Which red blood cells are Plasmodium falciparum-infected, and which are of indeterminate infection status?
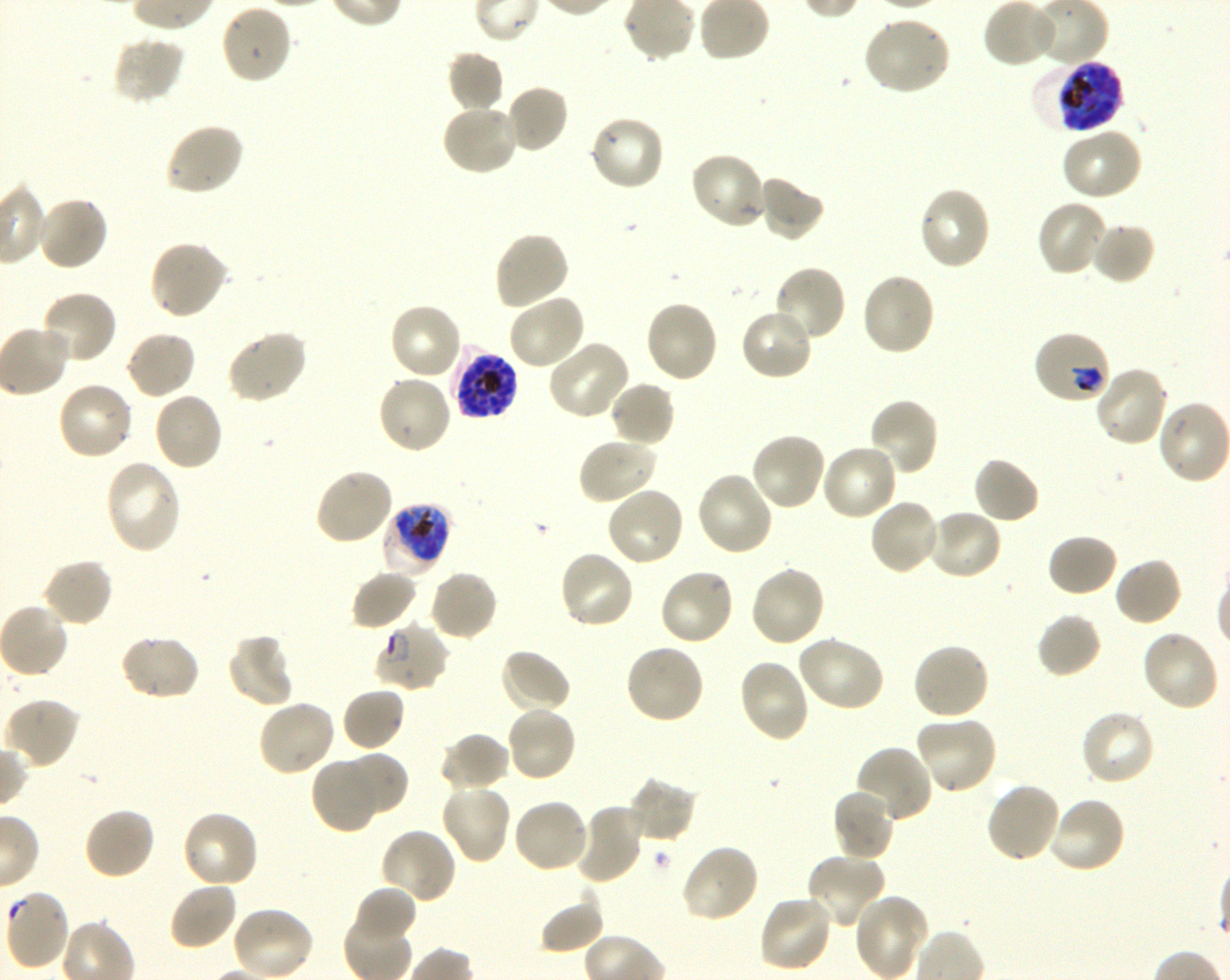

Approximate bounding boxes as [x1, y1, x2, y2] in pixels. Not every red blood cell is marked. A life-cycle stage — or a range of stages, where the recorded stages span more than one — follows each staged infected red blood cell.
Infected red blood cells: [1034, 58, 1124, 134] late trophozoite to late schizont; [1032, 330, 1112, 406] early trophozoite to early schizont; [453, 349, 518, 420] schizont; [380, 504, 451, 579] late trophozoite to late schizont; [373, 622, 450, 693] early ring to late trophozoite.
Red blood cells of indeterminate infection status: [2, 890, 69, 974].

locations of uninfected red blood cells = [220, 3, 294, 85], [862, 14, 952, 97], [112, 36, 186, 106], [447, 51, 504, 114], [503, 84, 569, 155], [441, 102, 519, 177], [588, 114, 666, 192], [164, 122, 245, 197], [1060, 127, 1143, 201], [687, 152, 767, 231], [757, 174, 825, 242], [917, 186, 993, 272], [34, 194, 109, 272], [1035, 199, 1111, 278], [1091, 221, 1156, 285], [493, 230, 570, 311], [148, 239, 229, 320], [772, 265, 847, 343], [860, 271, 936, 358], [39, 290, 118, 368], [506, 291, 587, 371], [643, 300, 719, 384], [388, 301, 464, 381], [739, 308, 814, 382], [125, 329, 197, 400], [226, 329, 308, 404], [546, 338, 632, 421], [1092, 365, 1170, 448], [376, 374, 454, 455], [55, 380, 134, 462], [608, 380, 676, 449], [151, 391, 224, 472], [867, 397, 939, 477], [750, 432, 828, 512], [577, 436, 658, 505], [819, 443, 898, 522], [971, 456, 1041, 525], [103, 459, 182, 554], [313, 466, 395, 546], [695, 471, 774, 557], [605, 485, 686, 568], [868, 497, 941, 575], [925, 507, 1003, 581], [1046, 532, 1119, 598], [558, 549, 635, 630], [42, 557, 114, 629], [1114, 557, 1183, 628], [748, 565, 827, 649], [657, 567, 736, 647], [427, 569, 499, 642], [350, 570, 419, 631], [1035, 612, 1102, 679], [1141, 629, 1220, 712], [118, 633, 201, 702], [227, 634, 295, 708], [796, 635, 885, 712], [911, 641, 991, 721], [623, 642, 705, 726], [498, 647, 573, 714], [737, 658, 811, 743], [341, 687, 406, 752], [3, 697, 81, 769], [257, 699, 337, 777], [506, 705, 578, 783], [1078, 709, 1156, 788], [914, 715, 998, 795], [439, 732, 511, 793], [854, 745, 934, 826], [340, 750, 409, 817], [311, 756, 383, 834], [628, 775, 699, 843], [985, 781, 1062, 864], [439, 782, 512, 865], [833, 788, 897, 863], [1047, 796, 1127, 874], [511, 798, 590, 874], [573, 804, 645, 886], [83, 807, 156, 882], [180, 808, 260, 889], [379, 827, 457, 904], [680, 843, 760, 924], [805, 853, 887, 930], [167, 880, 239, 950], [354, 886, 417, 944], [538, 893, 604, 955], [852, 895, 931, 979], [757, 896, 833, 973], [230, 906, 314, 980]
stain = Giemsa
field of view = single
preparation = thin blood film
donor blood group = O+
culture = shaking in-vitro Plasmodium falciparum strain 3D7
image size = 1230×980 pixels
objective = 100x, oil immersion, numerical aperture 1.30